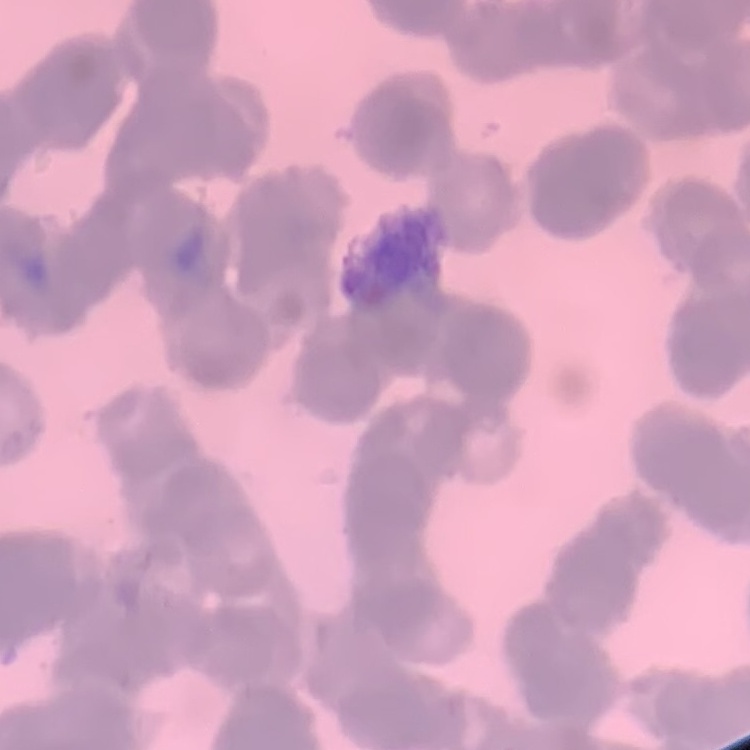
erythrocyte morphology = rouleaux formation
image type = one tile cut from a larger photomicrograph
preparation = thin blood smear
stain = Field's or Giemsa